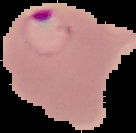
Result: Plasmodium parasites identified. From a thin blood film. The area outside the segmented cell region is set to black. Image is 136×133 pixels.